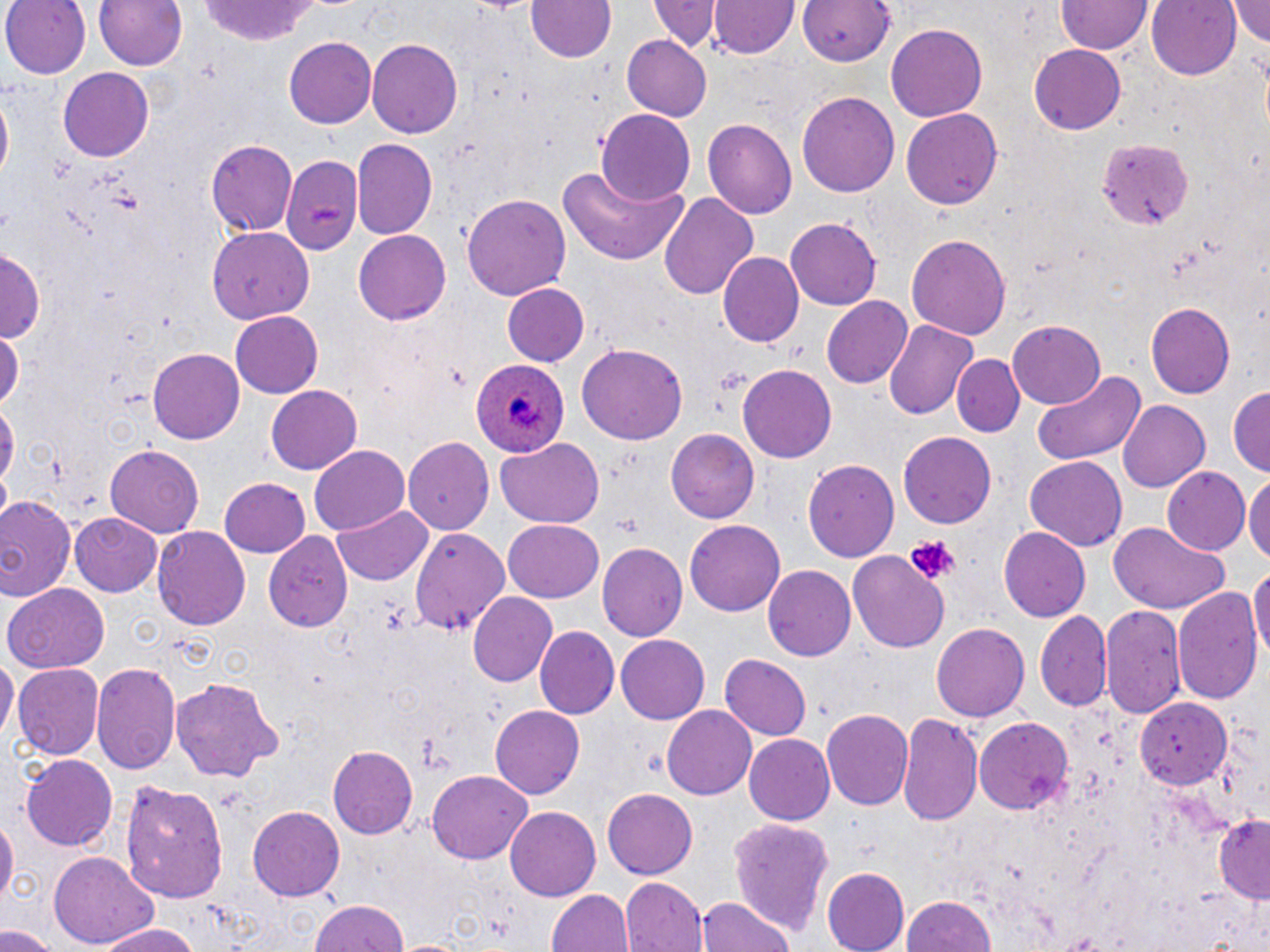

{
  "slide_level_diagnosis": "Plasmodium ovale",
  "modality": "light microscopy",
  "plasmodium_ovale_infected_red_blood_cell_locations": "approximate bounding boxes as (x1, y1, x2, y2) in pixels: (469, 359, 569, 460)",
  "stain": "May-Grünwald-Giemsa",
  "field_of_view": "single",
  "uninfected_red_blood_cell_locations": "approximate bounding boxes as (x1, y1, x2, y2) in pixels: (0, 0, 91, 80), (92, 0, 186, 73), (523, 0, 617, 65), (710, 0, 798, 59), (1055, 0, 1152, 55), (1147, 0, 1243, 79), (1229, 0, 1270, 47), (195, 1, 325, 45), (652, 1, 718, 53), (798, 1, 894, 69), (887, 22, 990, 122), (621, 36, 711, 119), (283, 37, 375, 129), (368, 38, 462, 139), (1028, 45, 1128, 134), (57, 66, 154, 160), (798, 89, 898, 195), (900, 108, 1004, 210), (597, 110, 694, 205), (704, 118, 796, 222), (1095, 137, 1196, 231), (204, 138, 298, 236), (353, 138, 436, 239), (280, 154, 361, 250), (556, 162, 691, 264), (462, 193, 570, 303), (658, 193, 759, 303), (785, 217, 881, 309), (206, 226, 313, 324), (354, 230, 451, 324), (906, 233, 1011, 340), (1, 246, 42, 345), (718, 252, 804, 347), (501, 283, 591, 367), (822, 296, 913, 389), (1145, 304, 1235, 397), (232, 313, 323, 397), (884, 319, 976, 421), (1006, 321, 1105, 410), (0, 325, 22, 412), (576, 343, 689, 445), (147, 348, 245, 444), (951, 353, 1025, 435), (738, 363, 836, 460), (1030, 368, 1146, 468), (1229, 382, 1270, 476), (265, 386, 361, 474), (0, 394, 17, 500), (1118, 399, 1211, 491), (666, 430, 759, 524), (899, 433, 996, 528), (404, 437, 494, 534), (496, 439, 605, 528), (104, 442, 204, 537), (310, 447, 409, 536), (1023, 456, 1129, 552), (803, 457, 900, 562), (1011, 457, 1109, 622), (1162, 465, 1252, 555), (1245, 471, 1270, 569), (218, 478, 309, 558), (0, 496, 78, 603), (332, 504, 434, 586), (69, 512, 163, 597), (503, 517, 605, 602), (685, 519, 785, 617), (1106, 522, 1232, 616), (409, 524, 511, 638), (152, 526, 249, 631), (998, 526, 1090, 622), (264, 533, 353, 631), (597, 543, 687, 643), (848, 552, 950, 653), (1250, 563, 1269, 665), (766, 565, 857, 660), (5, 585, 110, 672), (1173, 586, 1262, 709), (468, 593, 559, 689), (1101, 604, 1184, 719), (1035, 613, 1112, 714), (931, 622, 1029, 722), (533, 627, 620, 720), (615, 635, 709, 725), (0, 655, 17, 743), (721, 655, 810, 741), (91, 662, 180, 777), (12, 664, 103, 763), (169, 676, 285, 782), (1135, 696, 1231, 789), (487, 705, 585, 800), (661, 705, 757, 800), (821, 708, 912, 812), (900, 712, 984, 828), (974, 718, 1073, 816), (743, 733, 834, 824), (328, 745, 419, 839), (21, 756, 118, 852), (428, 769, 534, 863), (120, 778, 233, 903), (603, 787, 699, 879), (247, 805, 345, 901), (505, 806, 599, 902), (1211, 813, 1270, 902), (0, 815, 16, 908), (728, 816, 835, 938), (49, 853, 156, 950), (823, 867, 909, 951), (621, 876, 707, 952), (546, 889, 634, 952), (900, 894, 996, 952), (696, 896, 796, 952), (308, 897, 412, 952), (96, 923, 201, 952), (0, 925, 59, 952)",
  "preparation": "thin blood film",
  "image_size": "1270×952 pixels",
  "platelet_locations": "approximate bounding boxes as (x1, y1, x2, y2) in pixels: (904, 537, 957, 585)",
  "magnification": "1000x"
}